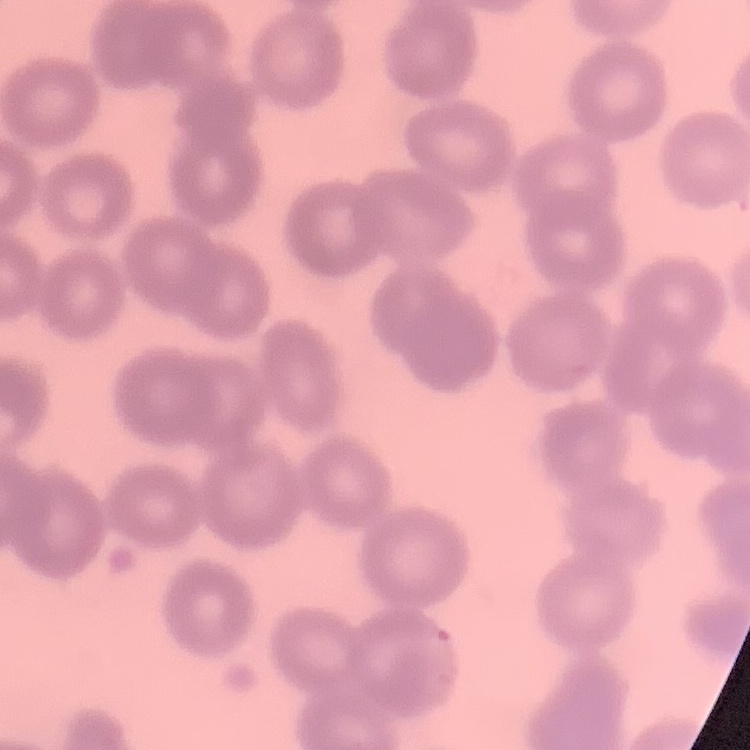
erythrocyte morphology = no rouleaux formation
image type = one tile cut from a larger photomicrograph
stain = Field's or Giemsa
preparation = thin blood film